Point out each Plasmodium parasite.
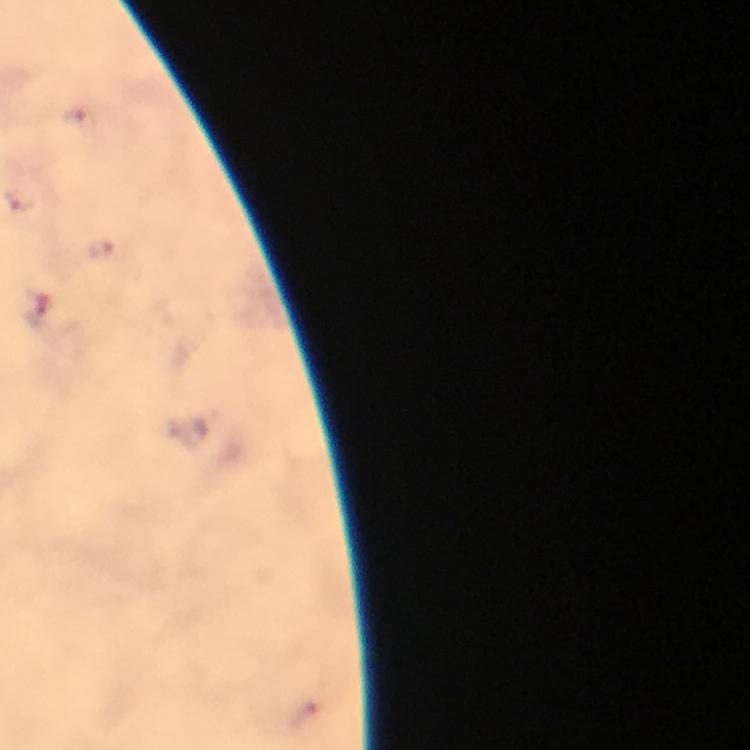

Approximate centers as {x, y} in pixels.
Plasmodium parasites: {78, 114}, {38, 309}.

Immersion oil applied. A crop from one field of view. From a malaria diagnostic workup. Thick blood film. At 100x magnification. Image is 750×750 pixels. Giemsa stain. Photographed through the microscope with a smartphone camera.